Locate and identify every blood parasite.
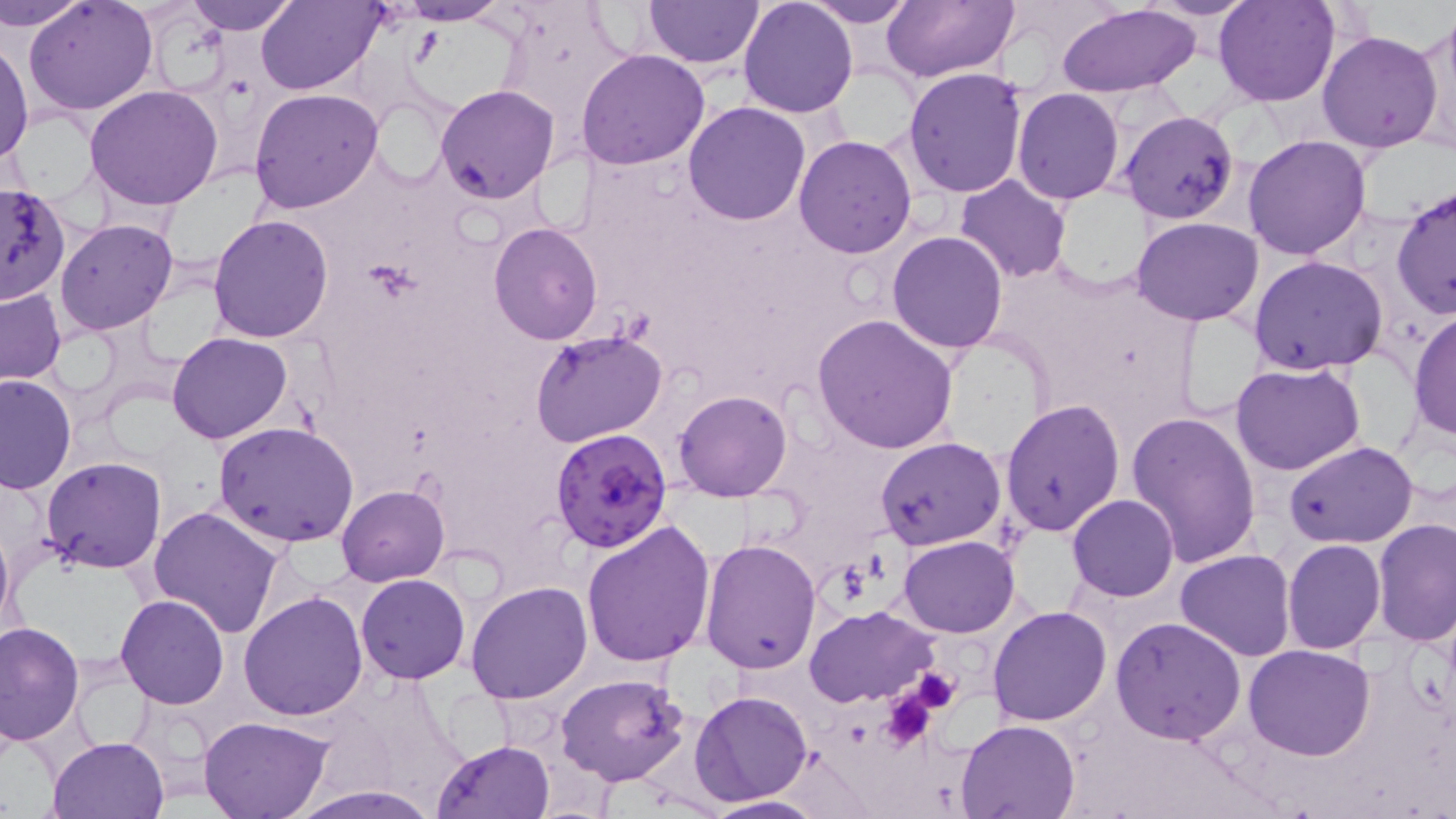
Approximate bounding boxes as (x1,y1)-(x2,y2) corner pairs in pixels.
Plasmodium falciparum-infected red blood cells: (549,428)-(673,553).
No Plasmodium ovale, Plasmodium malariae, Plasmodium vivax, Babesia divergens, or Trypanosoma brucei observed.

Summary:
  - Uninfected red blood cell locations: (3,0)-(91,32), (25,0)-(157,116), (184,0)-(300,34), (257,0)-(383,94), (390,0)-(514,24), (643,0)-(764,70), (804,0)-(915,27), (880,0)-(1019,82), (1144,0)-(1262,20), (1214,0)-(1339,107), (737,1)-(857,118), (1056,3)-(1203,98), (1411,14)-(1456,155), (1316,30)-(1444,154), (0,38)-(34,165), (577,49)-(711,170), (903,67)-(1029,196), (85,84)-(223,211), (435,84)-(559,203), (248,87)-(383,213), (1012,88)-(1124,205), (369,92)-(455,188), (683,101)-(812,224), (1120,110)-(1240,224), (1242,133)-(1373,260), (793,134)-(919,258), (955,175)-(1071,285), (1391,182)-(1455,322), (1,184)-(69,306), (208,213)-(336,342), (1131,217)-(1263,325), (55,218)-(178,335), (488,222)-(603,344), (887,230)-(1008,352), (1249,255)-(1390,373), (1,287)-(65,384), (1408,310)-(1456,442), (814,313)-(959,453), (530,328)-(667,448), (167,331)-(293,444), (1231,361)-(1367,475), (0,373)-(76,493), (674,389)-(793,501), (1000,400)-(1126,538), (1125,410)-(1261,567), (213,421)-(359,548), (875,437)-(1006,553), (1285,440)-(1418,549), (41,456)-(165,573), (337,484)-(450,586), (1068,494)-(1178,602), (148,506)-(286,639), (1374,518)-(1456,647), (580,519)-(715,670), (1,522)-(17,643), (898,535)-(1020,636), (698,536)-(821,674), (1283,540)-(1384,654), (1175,550)-(1295,662), (356,573)-(470,684), (466,581)-(593,703), (239,590)-(368,721), (115,594)-(230,709), (805,606)-(938,708), (987,606)-(1111,727), (1111,616)-(1247,744), (0,622)-(85,746), (1244,643)-(1376,761), (556,675)-(692,788), (689,690)-(814,807), (198,717)-(333,819), (954,718)-(1080,819), (48,736)-(171,819), (432,739)-(554,819), (290,787)-(445,818), (698,795)-(829,817)
  - Platelet locations: (904,667)-(962,714), (880,689)-(941,750)
  - Slide-level diagnosis: Plasmodium falciparum
  - Stain: May-Grünwald-Giemsa
  - Modality: light microscopy
  - Image size: 1456×819 pixels
  - Field of view: single
  - Preparation: thin blood smear
  - Magnification: 1000x